State the blood parasite species.
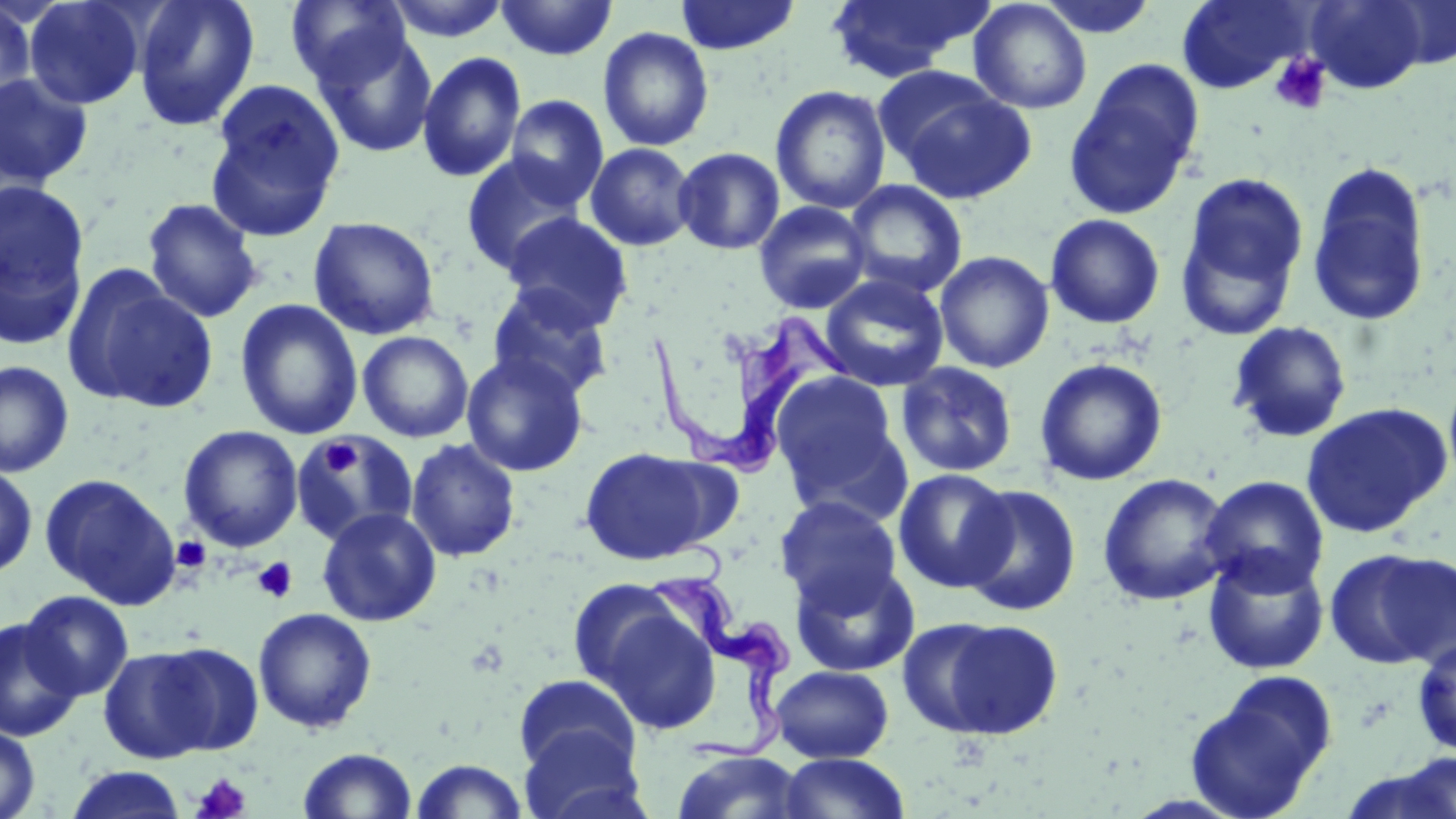

Trypanosoma brucei.

preparation: thin blood film
uninfected_red_blood_cell_locations: 'approximate bounding boxes as (x1,y1)-(x2,y2) corner pairs in pixels: (132,0)-(260,132), (285,0)-(413,90), (383,0)-(515,43), (496,0)-(618,61), (675,0)-(801,55), (825,0)-(992,81), (969,0)-(1092,114), (1038,0)-(1158,40), (1177,0)-(1311,93), (1305,0)-(1431,94), (1378,0)-(1456,70), (22,1)-(148,110), (0,3)-(36,116), (597,26)-(714,152), (311,27)-(438,159), (416,51)-(526,183), (1065,61)-(1204,218), (0,72)-(94,190), (204,79)-(347,239), (889,80)-(1037,205), (770,85)-(892,214), (504,95)-(609,208), (585,142)-(698,251), (673,146)-(785,255), (460,153)-(587,276), (1306,161)-(1432,328), (1176,172)-(1308,337), (1,179)-(91,332), (844,179)-(967,298), (142,197)-(265,324), (753,201)-(873,314), (501,213)-(632,331), (1045,213)-(1166,329), (308,216)-(441,340), (934,251)-(1054,373), (65,266)-(217,414), (820,274)-(949,392), (486,283)-(614,402), (235,298)-(363,439), (1227,321)-(1353,444), (357,331)-(474,443), (461,351)-(589,477), (1034,357)-(1168,486), (0,360)-(74,477), (895,362)-(1019,478), (770,371)-(905,511), (1301,403)-(1452,538), (179,425)-(303,552), (291,432)-(419,545), (405,438)-(521,562), (579,446)-(724,566), (0,463)-(38,579), (893,468)-(1015,593), (39,473)-(181,609), (1096,473)-(1233,606), (1200,475)-(1330,595), (958,484)-(1082,617), (774,495)-(903,614), (317,507)-(441,627), (1325,547)-(1455,671), (1203,550)-(1330,675), (790,559)-(920,678), (566,577)-(690,697), (20,590)-(133,700), (594,602)-(723,736), (252,607)-(378,733), (0,616)-(83,743), (924,616)-(1065,741), (1412,637)-(1456,757), (144,642)-(265,755), (98,645)-(221,763), (771,665)-(893,763), (1186,672)-(1336,817), (513,674)-(641,777), (0,721)-(41,819), (518,725)-(646,819), (298,747)-(418,819), (670,751)-(808,819), (1393,752)-(1455,819), (777,753)-(910,819), (408,759)-(529,819), (65,766)-(188,818)'
field_of_view: one of a larger specimen
image_size: 1456×819 pixels
trypanosoma_brucei_locations: 'approximate bounding boxes as (x1,y1)-(x2,y2) corner pairs in pixels: (647,302)-(852,476), (648,569)-(789,764)'
platelet_locations: 'approximate bounding boxes as (x1,y1)-(x2,y2) corner pairs in pixels: (1269,53)-(1332,116), (321,438)-(362,477), (171,536)-(211,573), (253,557)-(297,604), (190,772)-(252,819)'
modality: optical microscopy
stain: May-Grünwald-Giemsa
magnification: 1000x